Report the malaria status of this cell.
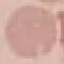
It is uninfected.

image type = cell patch, automatically extracted from a larger field of view and resized to 64 × 64 pixels
capture = smartphone through the microscope eyepiece
preparation = thin blood smear
stain = Giemsa